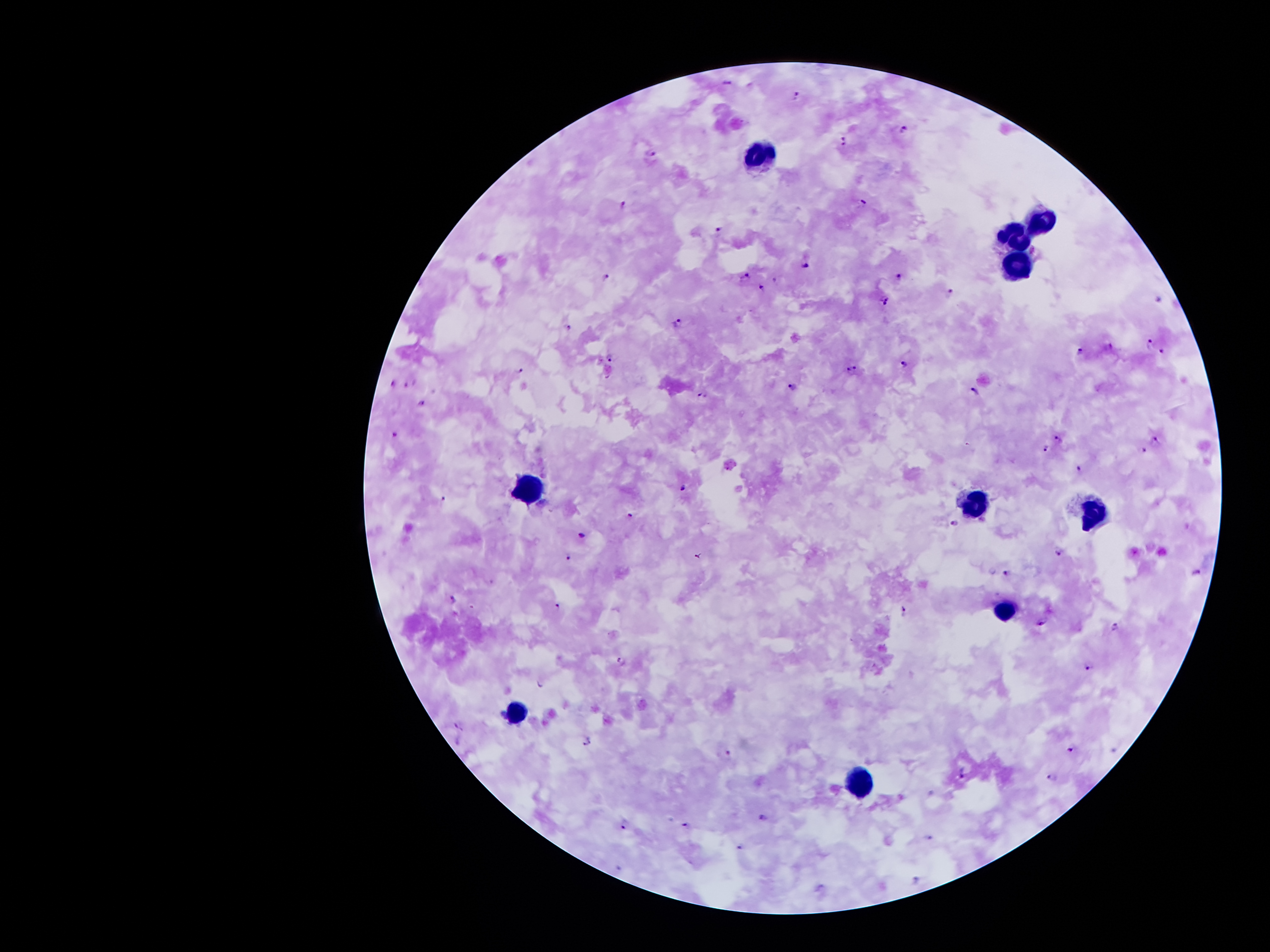
image_size: 1270×952 pixels
stain: Giemsa
leukocyte_locations: 'approximate centers as [x, y] in pixels: [759, 155], [1038, 221], [1011, 234], [1014, 273], [527, 488], [977, 495], [1094, 509], [1005, 607], [518, 711], [861, 784]'
magnification: 100x
field_of_view: single
patient_malaria_status: positive for Plasmodium falciparum
malaria_parasite_locations: 'approximate centers as [x, y] in pixels: [729, 81], [797, 96], [904, 129], [846, 140], [650, 153], [624, 204], [863, 204], [720, 227], [805, 265], [899, 276], [744, 277], [605, 278], [774, 281], [762, 286], [949, 293], [1159, 299], [885, 300], [679, 323], [567, 324], [1149, 342], [1081, 351], [1162, 353], [609, 356], [905, 363], [852, 367], [519, 370], [410, 382], [392, 384], [792, 386], [975, 392], [704, 397], [421, 402], [396, 433], [1058, 440], [1156, 441], [1045, 447], [1143, 449], [1078, 469], [683, 487], [443, 499], [631, 516], [955, 523], [583, 534], [699, 554], [1058, 554], [568, 557], [1198, 571], [1009, 572], [453, 598], [557, 606], [902, 608], [1041, 623], [1117, 627], [621, 660], [1088, 666], [540, 683], [459, 726], [586, 740], [1071, 749], [727, 753], [963, 774], [1051, 778], [763, 816], [626, 824], [686, 825], [929, 838], [740, 847], [917, 880]'
capture: smartphone through the microscope eyepiece
preparation: thick blood film